Report the malaria status of this cell.
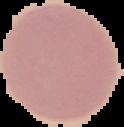

It is uninfected.

From a thin blood smear. The area outside the segmented cell region is set to black. Image is 124×127 pixels.